Name the parasite shown.
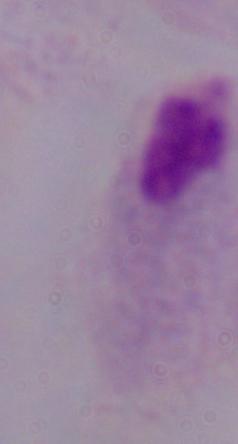

A trichomonad.

Summary:
  - Modality: micrograph
  - Magnification: 1000x